Describe the morphology of the erythrocytes.
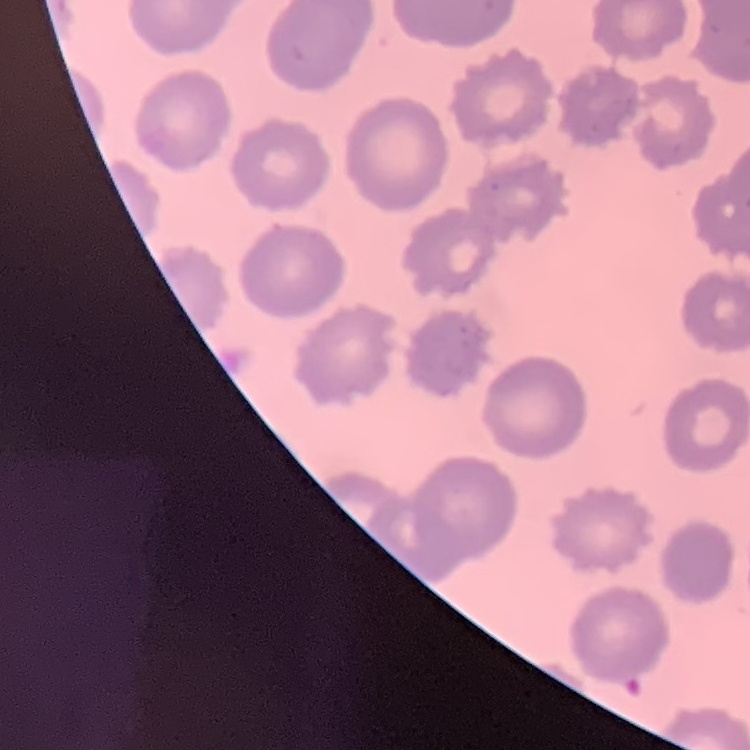

They show no rouleaux formation.

Field's or Giemsa stain. One tile cut from a larger photomicrograph. Thin blood smear.